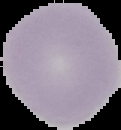
Result: negative for Plasmodium parasites. From a thin blood film. Cell region segmented out of the field of view; the surrounding area is masked to black. Image is 121×130 pixels.